Comment on the morphology of the erythrocytes.
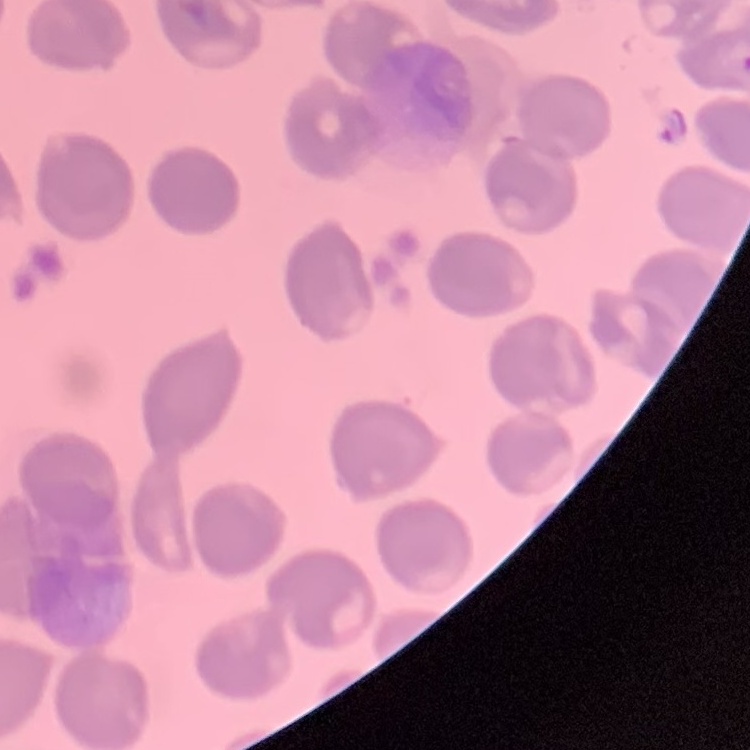

They show no rouleaux formation.

stain = Field's or Giemsa
image type = square crop of a larger photomicrograph
preparation = thin blood film